Give the position of every malaria parasite.
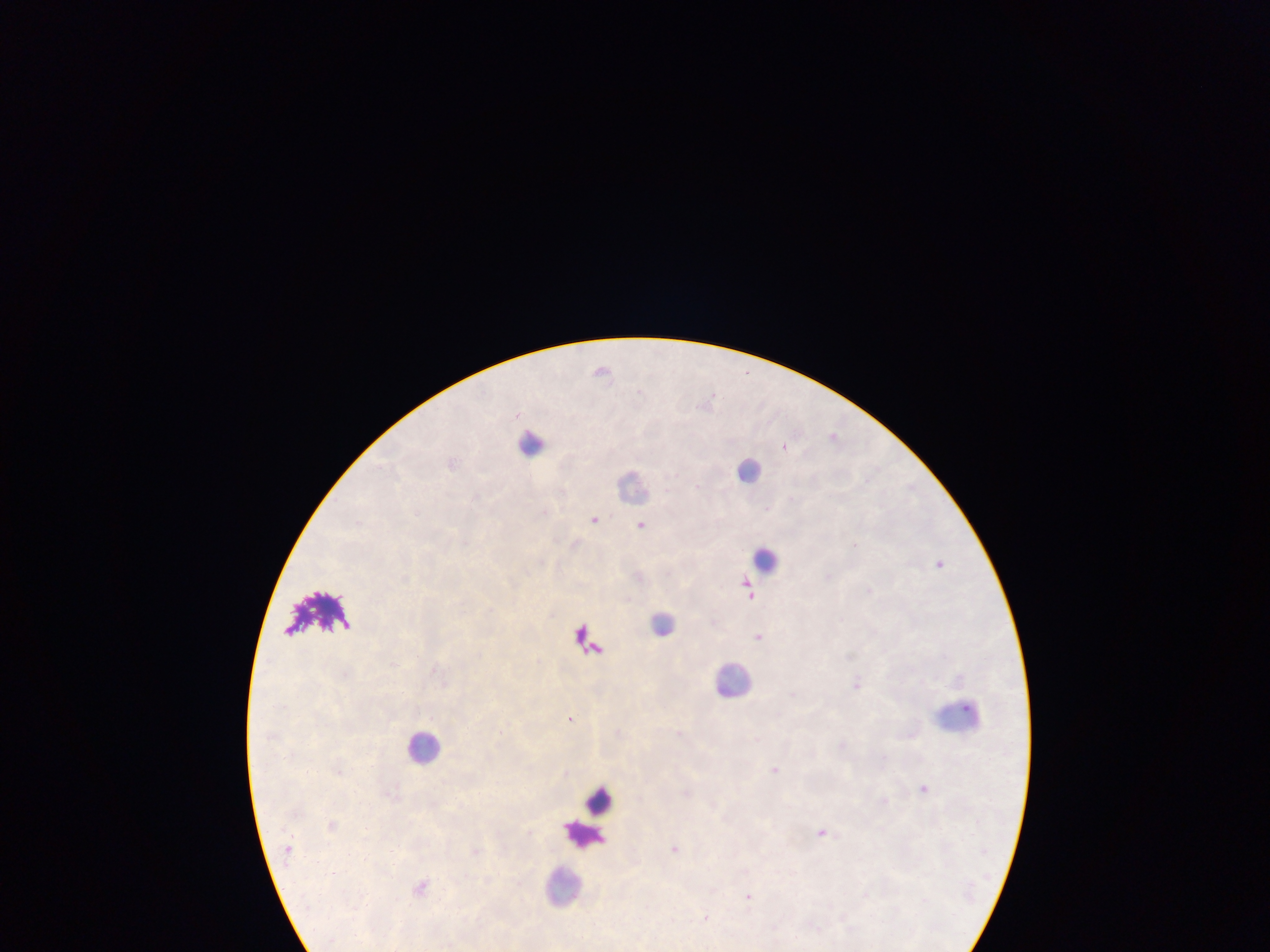

Approximate centers as (x, y) in pixels.
Malaria parasites: (603, 370), (834, 437), (785, 445), (595, 518), (641, 524), (940, 563), (829, 575), (749, 588), (869, 590), (759, 637), (857, 684), (571, 718), (680, 733), (845, 744), (775, 769), (566, 771), (924, 788), (884, 799), (823, 832), (676, 848), (421, 886), (750, 896), (705, 917).

Summary:
  - Leukocyte locations: (531, 443), (750, 469), (633, 483), (765, 559), (662, 622), (590, 642), (734, 679), (959, 716), (423, 746), (600, 799), (584, 833), (563, 885)
  - Preparation: thick blood film
  - Capture: mobile-phone photograph through a microscope
  - Image size: 1270×952 pixels
  - Field of view: single
  - Country: Ghana